Report the malaria status of this cell.
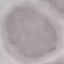

It is uninfected.

Summary:
  - Preparation: thin blood smear
  - Capture: smartphone camera at the microscope eyepiece
  - Image type: automatically extracted cell patch, resized to 64 × 64 pixels
  - Stain: Giemsa